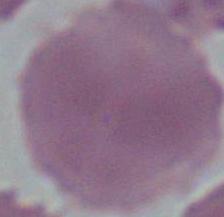
modality = photomicrograph
identification = red blood cell
magnification = 1000x